Classify this cell by malaria status.
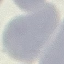
It is uninfected.

capture = smartphone through the microscope eyepiece
stain = Giemsa
preparation = thin blood film
image type = cell patch, automatically extracted from a larger field of view and resized to 64 × 64 pixels